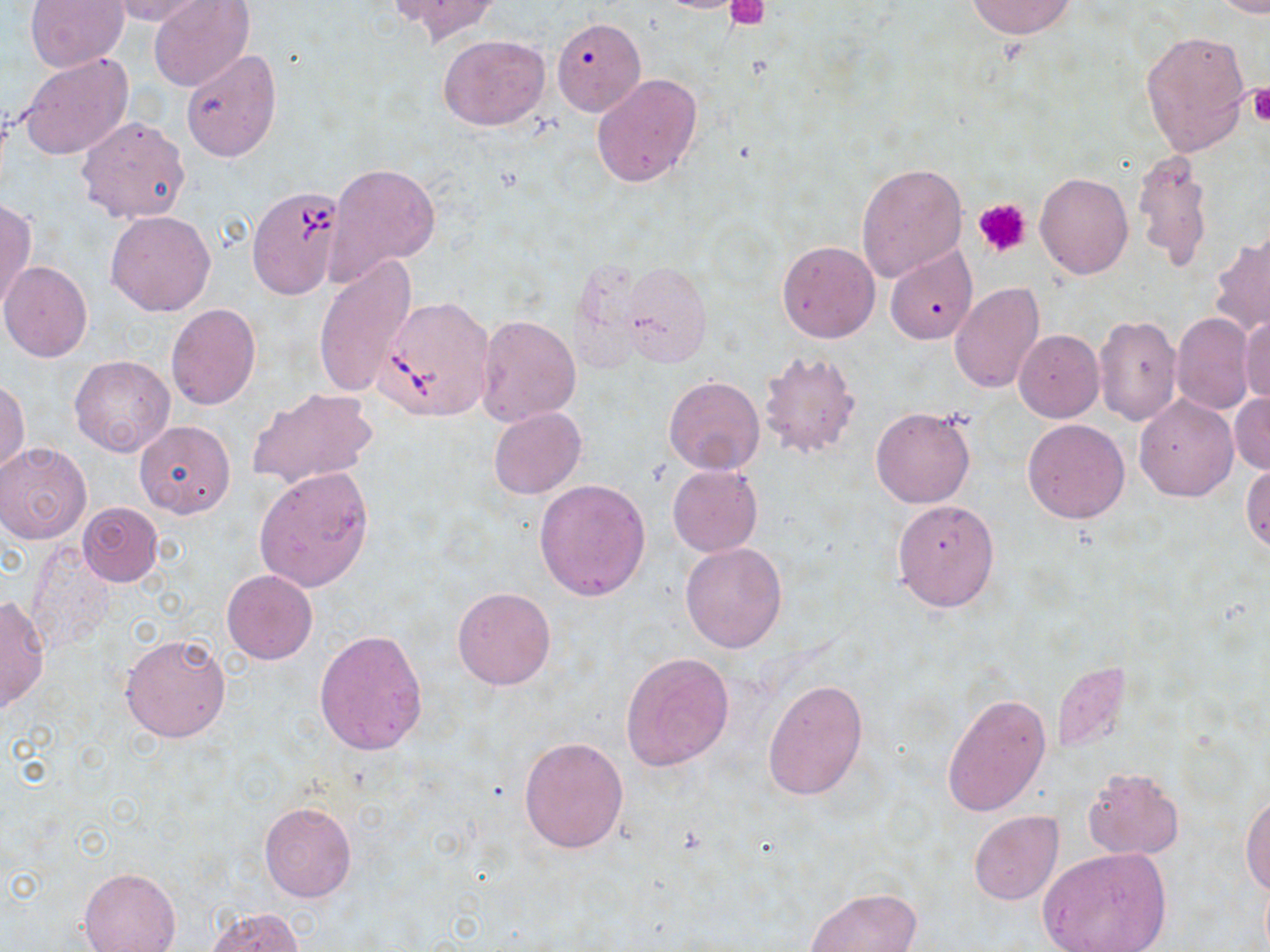

Approximate bounding boxes as (x1, y1, x2, y2) in pixels. Uninfected red blood cell locations: (27, 0, 129, 70), (103, 0, 210, 26), (388, 0, 500, 44), (966, 0, 1075, 38), (1211, 0, 1270, 17), (148, 1, 254, 91), (552, 19, 645, 116), (1139, 29, 1252, 156), (439, 34, 550, 131), (180, 48, 282, 161), (18, 52, 132, 161), (591, 73, 703, 188), (76, 115, 191, 223), (1134, 149, 1214, 274), (856, 161, 969, 282), (328, 164, 440, 276), (1034, 172, 1133, 279), (0, 198, 36, 313), (106, 211, 215, 316), (1211, 232, 1270, 337), (777, 239, 880, 343), (883, 246, 977, 345), (312, 255, 416, 401), (622, 262, 711, 365), (0, 263, 92, 362), (949, 283, 1044, 395), (166, 303, 261, 410), (1170, 312, 1255, 415), (1239, 313, 1270, 408), (476, 314, 580, 424), (1093, 314, 1182, 427), (1014, 330, 1103, 422), (756, 349, 861, 459), (69, 356, 175, 459), (663, 375, 765, 475), (0, 379, 29, 476), (246, 386, 378, 491), (1230, 392, 1270, 475), (1134, 394, 1238, 502), (870, 405, 975, 508), (488, 407, 585, 499), (1021, 419, 1129, 524), (135, 420, 235, 519), (0, 442, 91, 543), (1242, 463, 1270, 554), (668, 464, 762, 555), (253, 467, 374, 593), (533, 478, 651, 602), (891, 499, 999, 612), (76, 501, 165, 587), (679, 541, 788, 654), (25, 542, 117, 650), (222, 570, 317, 665), (452, 585, 557, 690), (0, 595, 49, 716), (313, 628, 429, 756), (120, 631, 232, 744), (621, 651, 735, 770), (762, 679, 868, 800), (941, 691, 1050, 818), (518, 736, 629, 854), (1082, 767, 1184, 858), (1242, 793, 1270, 896), (258, 801, 357, 903), (969, 812, 1062, 905), (1038, 847, 1171, 952), (78, 866, 181, 952), (805, 887, 923, 952), (205, 907, 304, 951). Platelet locations: (726, 0, 769, 28), (1248, 87, 1270, 126), (973, 198, 1032, 259). Babesia divergens-infected red blood cell locations: (247, 185, 346, 299), (375, 296, 496, 421). Slide-level diagnosis: Babesia divergens. Light microscopy. 1000x magnification. May-Grünwald-Giemsa stain. Single field of view. Thin blood smear. Image is 1270×952 pixels.